Name the cell type shown.
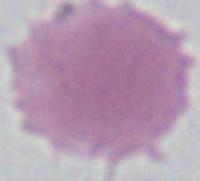
This is an erythrocyte.

magnification: 1000x
modality: micrograph